Report the malaria status of this cell.
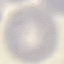
Uninfected.

stain = Giemsa
capture = smartphone through the microscope eyepiece
image type = automatically extracted cell patch, resized to 64 × 64 pixels
preparation = thin smear